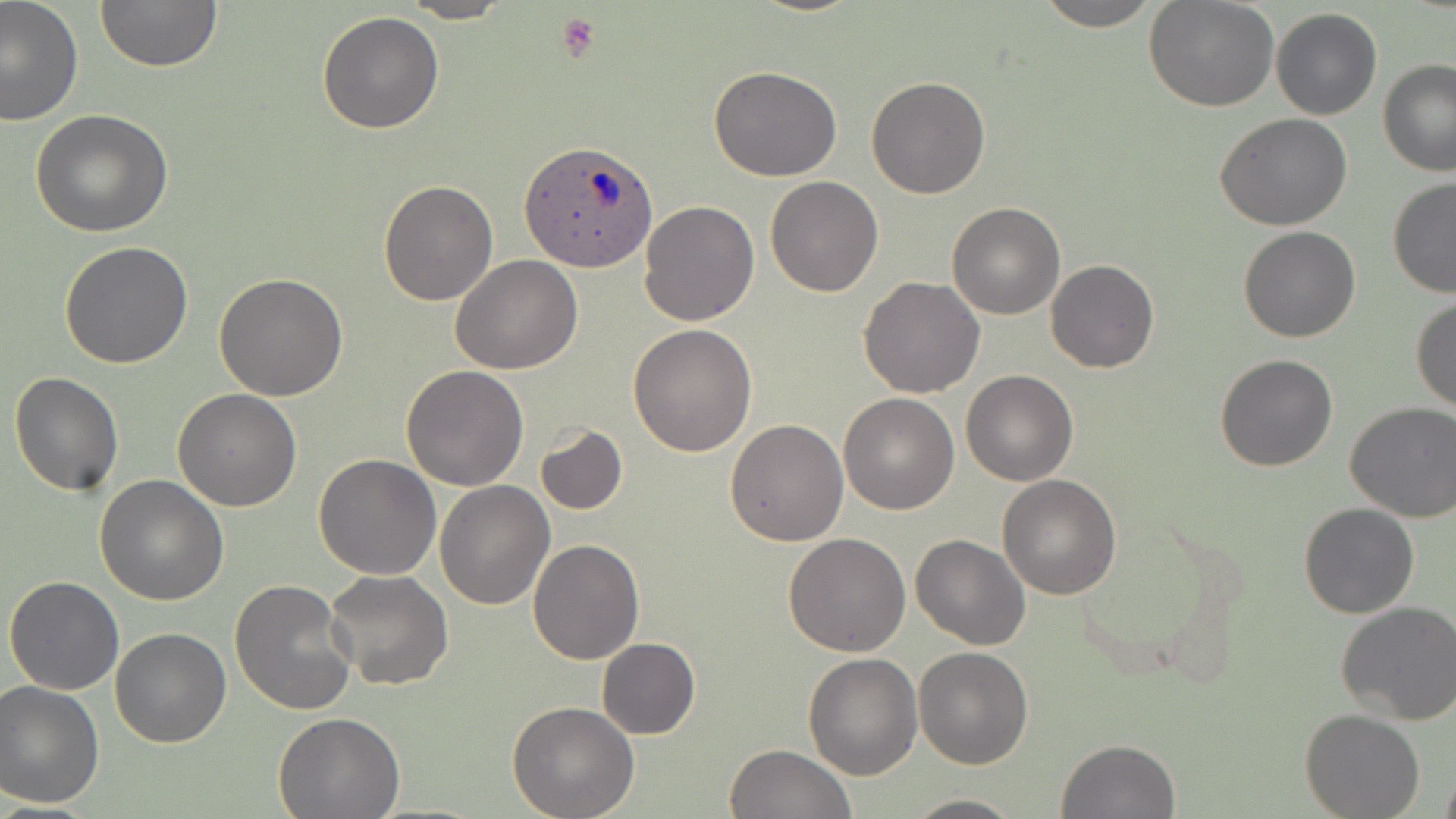

slide-level diagnosis = Plasmodium ovale
image size = 1456×819 pixels
uninfected red blood cell locations = approximate bounding boxes as [x1, y1, x2, y2] in pixels: [0, 0, 83, 126], [400, 0, 512, 23], [1033, 0, 1162, 30], [94, 1, 223, 73], [1145, 2, 1278, 112], [1271, 7, 1382, 121], [317, 11, 444, 134], [1379, 59, 1456, 178], [710, 66, 842, 183], [866, 76, 990, 199], [29, 110, 173, 239], [1214, 112, 1353, 229], [765, 176, 884, 296], [377, 178, 498, 304], [1387, 178, 1456, 300], [639, 200, 761, 326], [946, 201, 1065, 320], [1239, 226, 1361, 343], [60, 240, 194, 369], [451, 255, 584, 373], [1044, 259, 1159, 373], [213, 273, 348, 400], [858, 277, 985, 397], [1410, 296, 1456, 417], [628, 324, 758, 457], [1214, 353, 1339, 472], [401, 365, 530, 490], [960, 370, 1078, 486], [9, 372, 124, 495], [174, 389, 302, 511], [838, 393, 959, 514], [1345, 400, 1456, 522], [725, 419, 848, 546], [534, 425, 627, 515], [312, 454, 441, 578], [95, 474, 228, 606], [997, 475, 1122, 600], [435, 480, 556, 609], [1299, 503, 1420, 619], [783, 533, 911, 657], [910, 534, 1031, 649], [529, 537, 644, 664], [325, 569, 453, 692], [4, 575, 125, 695], [229, 579, 358, 716], [1335, 601, 1456, 725], [110, 628, 231, 747], [597, 638, 701, 739], [914, 646, 1034, 769], [802, 651, 922, 779], [0, 680, 104, 809], [506, 701, 640, 819], [273, 710, 403, 818], [1301, 710, 1423, 819], [1057, 738, 1180, 818], [725, 743, 855, 819], [1439, 765, 1456, 819], [902, 793, 1025, 818]
preparation = thin blood smear
stain = May-Grünwald-Giemsa
field of view = one of a larger specimen
Plasmodium ovale-infected red blood cell locations = approximate bounding boxes as [x1, y1, x2, y2] in pixels: [521, 141, 659, 273]
modality = optical microscopy
magnification = 1000x
platelet locations = approximate bounding boxes as [x1, y1, x2, y2] in pixels: [554, 11, 600, 62]